Assess this cell for malaria.
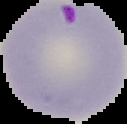
Parasitized.

{
  "preparation": "thin blood smear",
  "image_type": "cell region segmented out of the field of view; surrounding area masked to black",
  "image_size": "127×124 pixels"
}